Evaluate for malaria.
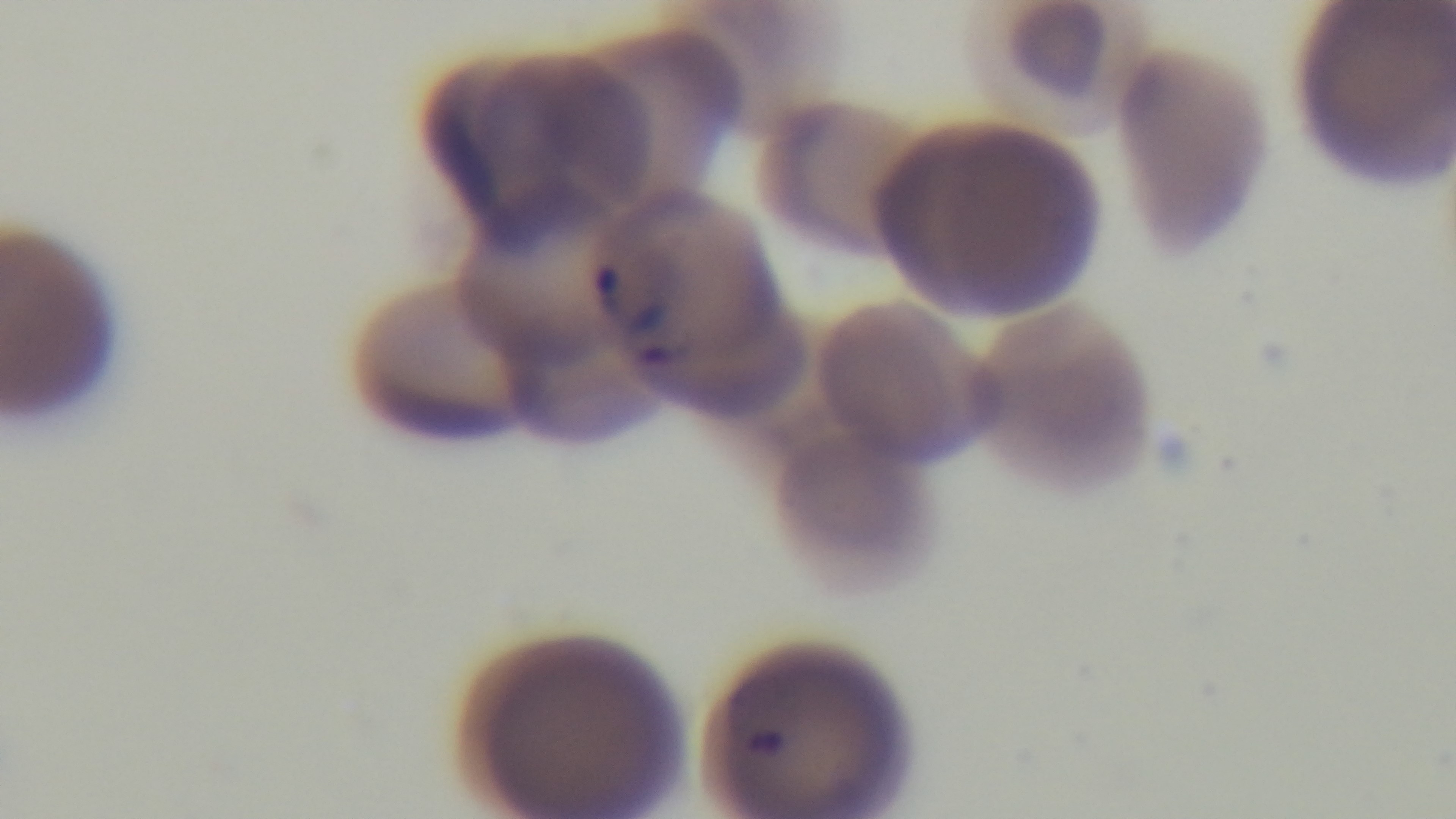

Positive.

Mounted 4K digital camera. Oil-immersion objective, 100x. Giemsa-stained. Preparation: thin smear. One field from the slide. Light microscopy.